State which parasite is depicted.
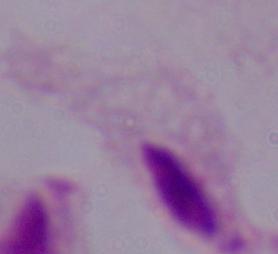

This is a trichomonad.

modality = micrograph
magnification = 1000x